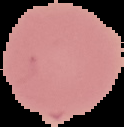
Summary:
  - Malaria status: uninfected
  - Image type: segmented cell region on a black background
  - Preparation: thin blood film
  - Image size: 124×127 pixels